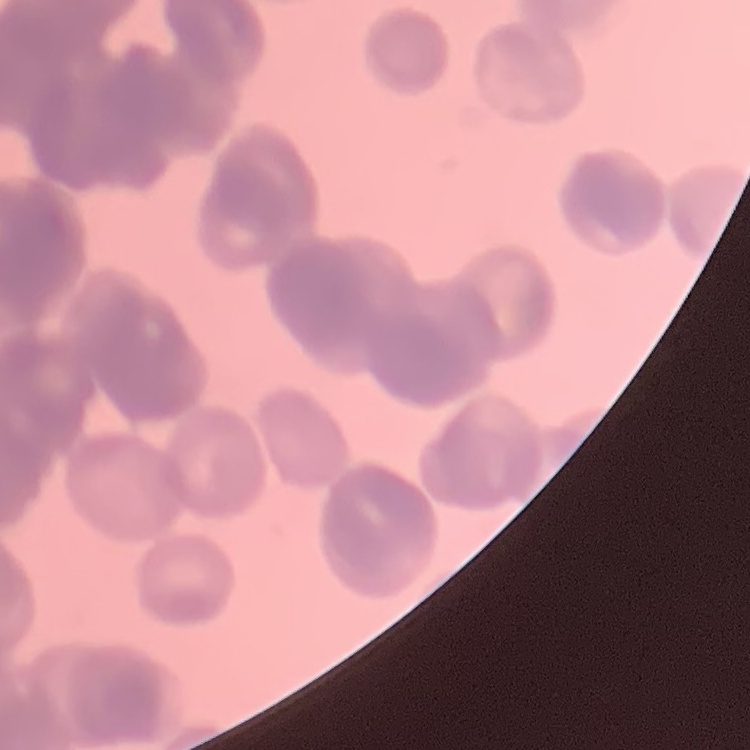
red blood cell morphology = rouleaux formation
image type = square crop of a larger photomicrograph
preparation = thin blood film
stain = Field's or Giemsa